Give the position of every Plasmodium parasite visible.
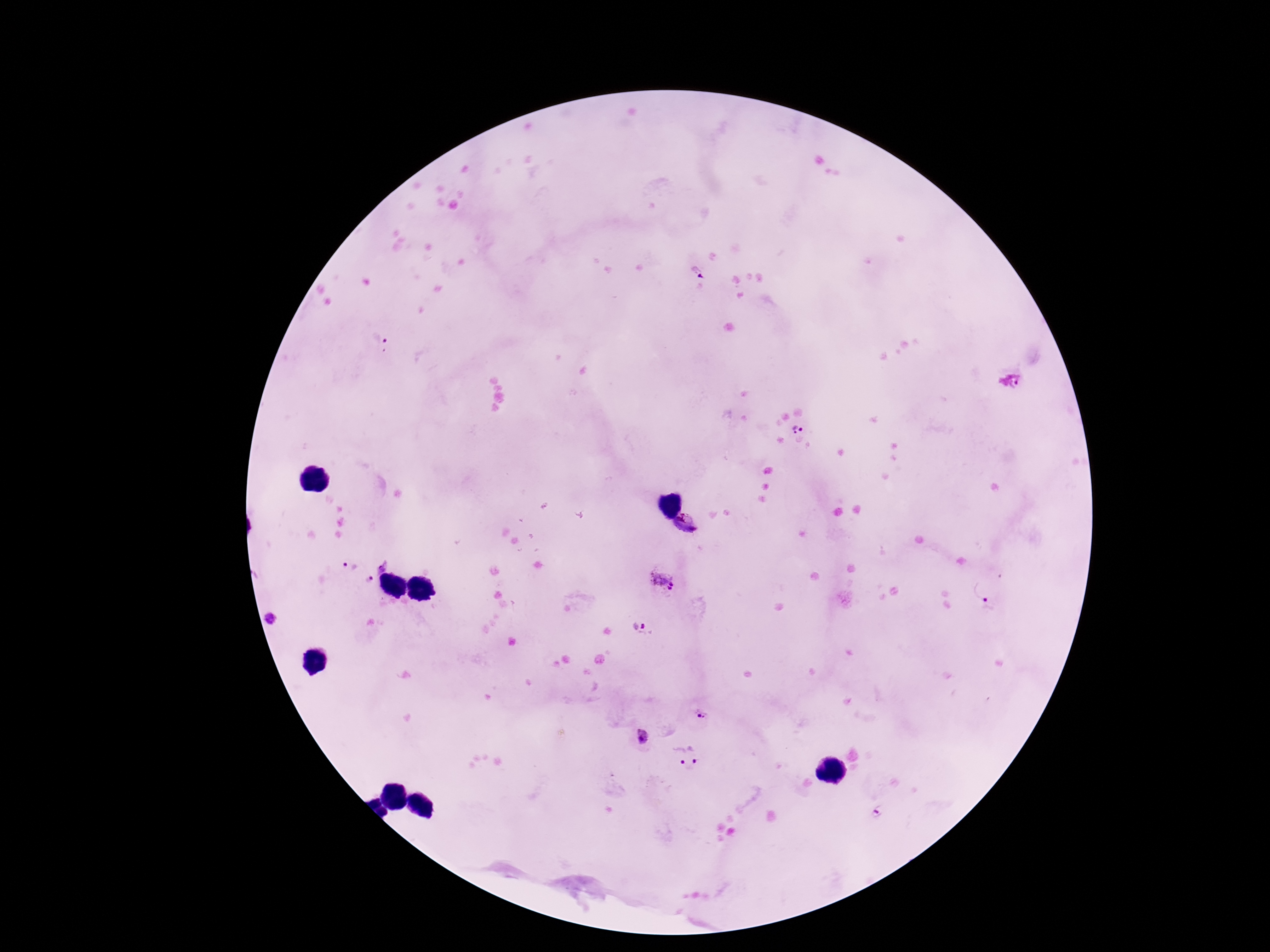

Approximate centers as {x, y} in pixels.
Plasmodium parasites: {697, 270}, {380, 343}, {1013, 383}, {797, 429}, {687, 525}, {381, 563}, {346, 565}, {368, 580}, {660, 580}, {983, 589}, {643, 625}, {702, 715}, {643, 736}, {698, 752}, {676, 755}, {878, 811}.

Thick blood smear. 100x magnification. Patient malaria status: positive. Smartphone photograph taken through the microscope eyepiece. Image is 1270×952 pixels. Single field of view. Giemsa-stained preparation.